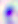
identification = Toxoplasma gondii
magnification = 400x
modality = micrograph